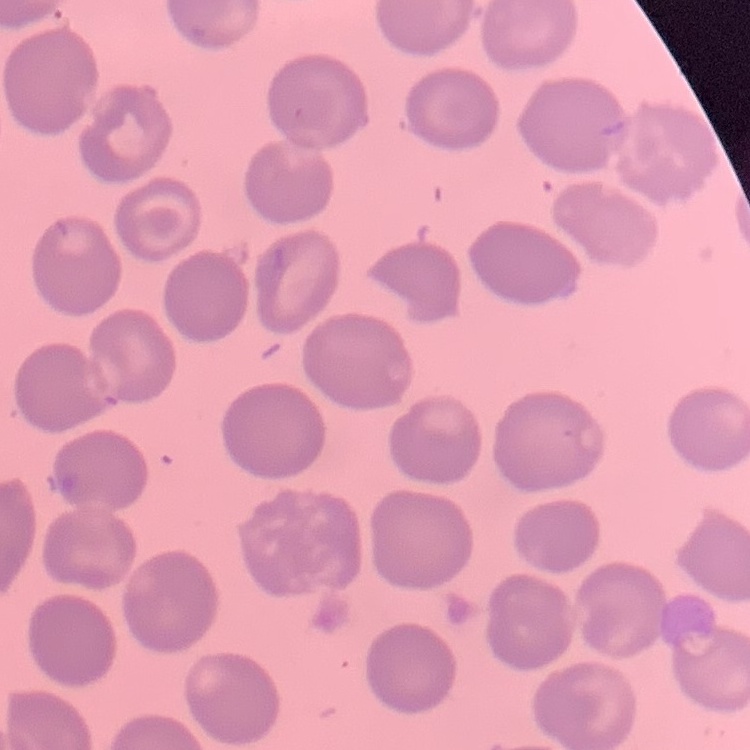

red blood cell morphology = no rouleaux formation
preparation = thin blood smear
stain = Field's or Giemsa
image type = square crop of a larger photomicrograph